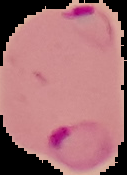
result: malaria parasites identified
image_type: segmented cell region with the area outside set to black
image_size: 127×175 pixels
preparation: thin blood film